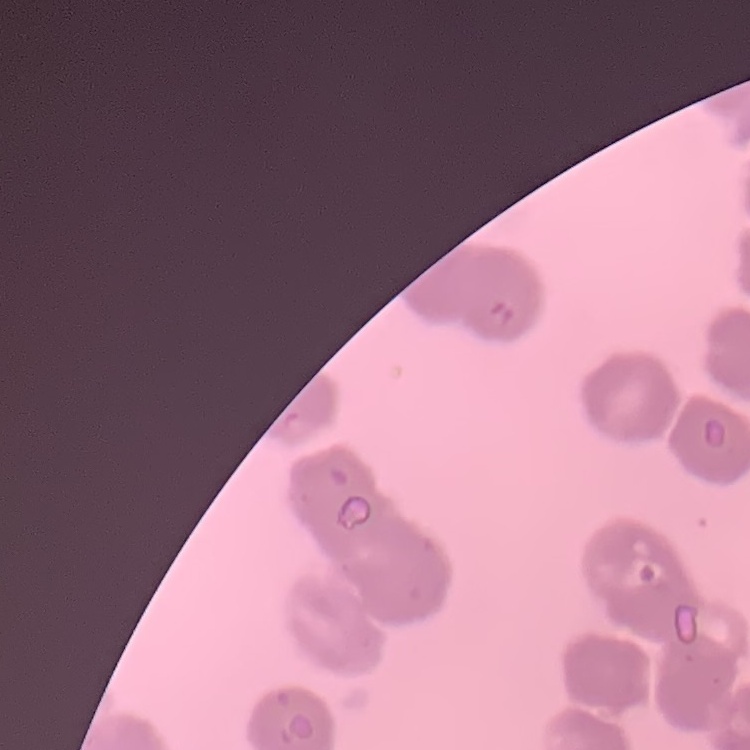 The red blood cells show rouleaux formation. Thin peripheral smear. Square crop of a larger photomicrograph. Field's or Giemsa stain.